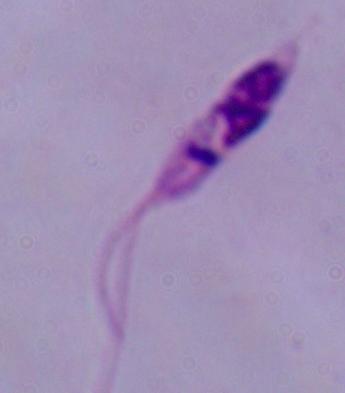
{
  "magnification": "1000x",
  "identification": "Leishmania",
  "modality": "photomicrograph"
}